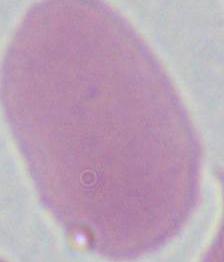
Summary:
  - Magnification: 1000x
  - Modality: photomicrograph
  - Identification: red blood cell